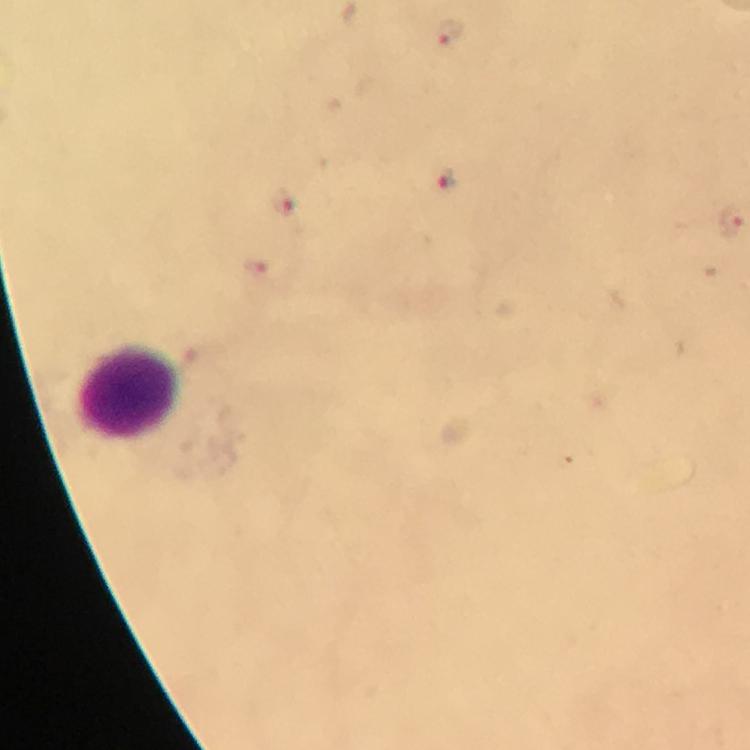
Approximate centers as [x, y] in pixels. Plasmodium parasite locations: [448, 35], [448, 180], [282, 205], [254, 267]. Leukocyte locations: [130, 394]. At 100x magnification. Immersion oil was used. From a malaria diagnostic workup. Image is 750×750 pixels. Giemsa-stained preparation. Smartphone photograph taken through a microscope. Thick blood smear. A crop from one field of view.